Assess this cell for malaria.
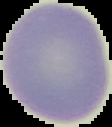
It is uninfected.

image type = cell region segmented out of the field of view; surrounding area masked to black
image size = 112×127 pixels
preparation = thin blood film